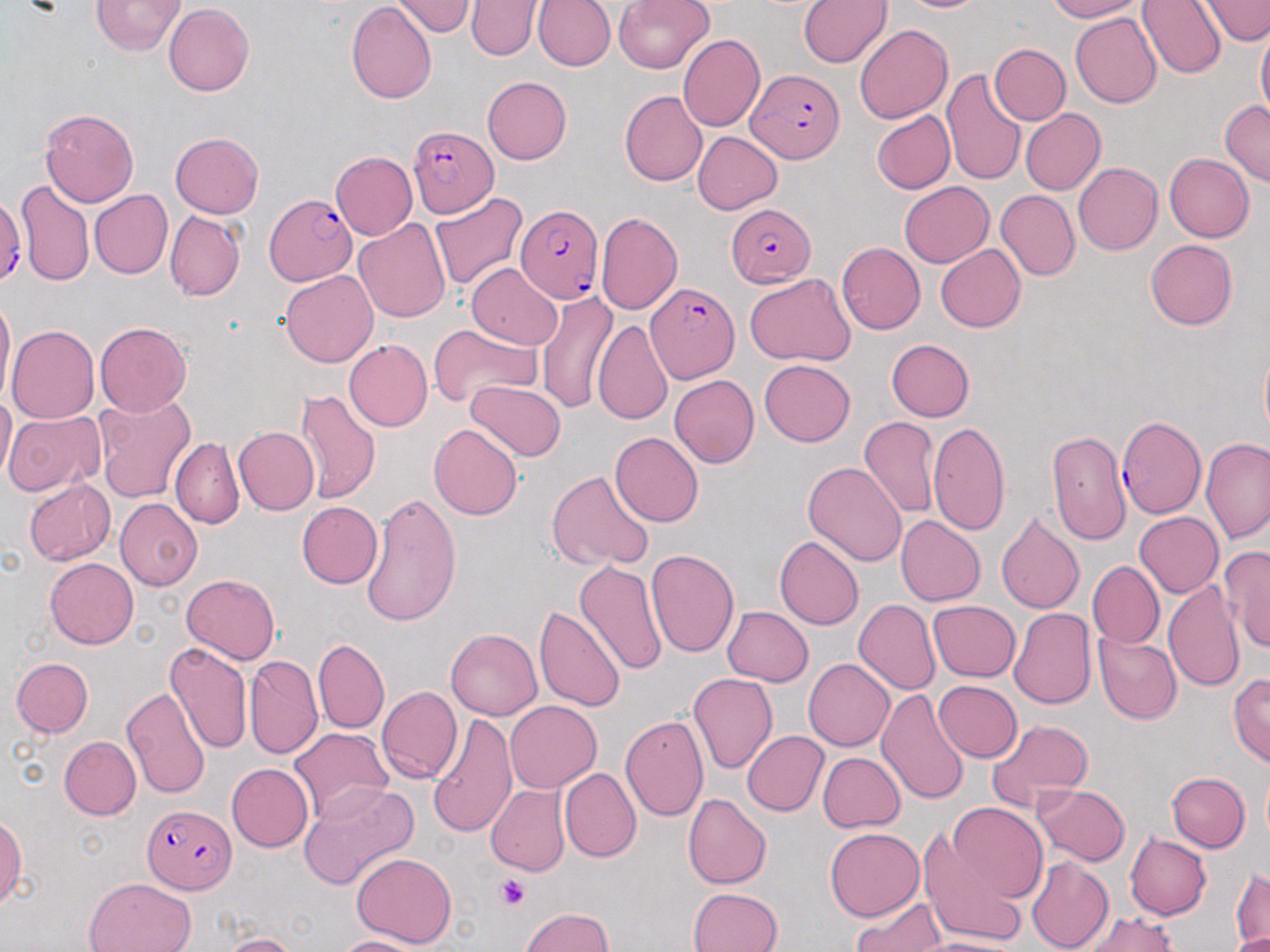
slide-level diagnosis = Plasmodium falciparum
field of view = one of a larger specimen
Plasmodium falciparum-infected red blood cell locations = approximate bounding boxes as (x1, y1, x2, y2) in pixels: (747, 69, 844, 164), (406, 125, 497, 218), (265, 194, 356, 285), (0, 197, 24, 284), (515, 203, 604, 302), (726, 203, 816, 285), (644, 282, 738, 383), (1116, 416, 1205, 519), (139, 805, 235, 892)
platelet locations = approximate bounding boxes as (x1, y1, x2, y2) in pixels: (494, 872, 529, 911)
preparation = thin blood film
uninfected red blood cell locations = approximate bounding boxes as (x1, y1, x2, y2) in pixels: (391, 0, 475, 37), (533, 0, 615, 71), (612, 0, 715, 74), (798, 0, 893, 68), (897, 0, 990, 13), (1045, 0, 1145, 22), (1138, 0, 1227, 78), (1199, 0, 1270, 46), (91, 1, 186, 55), (346, 1, 437, 104), (465, 1, 540, 60), (163, 3, 254, 96), (1070, 13, 1162, 108), (853, 24, 952, 124), (1256, 25, 1270, 127), (677, 35, 764, 132), (989, 44, 1070, 125), (942, 69, 1027, 187), (482, 77, 572, 165), (620, 90, 707, 186), (1220, 100, 1270, 187), (41, 107, 139, 207), (1020, 109, 1106, 195), (872, 110, 955, 194), (692, 130, 781, 214), (170, 131, 263, 217), (331, 150, 417, 241), (1164, 153, 1254, 242), (1073, 163, 1162, 255), (15, 179, 95, 288), (900, 182, 994, 267), (994, 189, 1079, 281), (89, 190, 172, 279), (429, 191, 527, 292), (165, 211, 245, 301), (595, 211, 683, 315), (354, 217, 451, 324), (1145, 239, 1238, 331), (837, 242, 925, 336), (936, 245, 1026, 332), (466, 264, 563, 349), (279, 270, 378, 368), (744, 273, 857, 368), (537, 289, 618, 415), (0, 294, 16, 406), (591, 320, 671, 425), (94, 322, 192, 417), (429, 323, 542, 411), (6, 325, 99, 424), (343, 339, 432, 432), (886, 339, 974, 422), (1260, 347, 1270, 442), (759, 359, 854, 447), (670, 375, 760, 468), (465, 379, 568, 462), (296, 389, 380, 502), (0, 393, 17, 482), (92, 394, 195, 503), (3, 410, 108, 498), (860, 414, 941, 519), (928, 421, 1010, 536), (429, 424, 523, 520), (233, 427, 319, 516), (1047, 429, 1130, 545), (610, 431, 703, 529), (171, 436, 244, 530), (1202, 437, 1270, 542), (802, 461, 907, 566), (546, 470, 654, 571), (23, 478, 115, 565), (358, 491, 461, 630), (115, 497, 203, 590), (296, 501, 383, 588), (995, 510, 1085, 615), (1134, 511, 1224, 597), (895, 515, 986, 606), (774, 535, 864, 630), (1220, 545, 1270, 652), (645, 549, 740, 658), (44, 558, 138, 648), (574, 559, 668, 677), (1088, 560, 1164, 648), (181, 573, 280, 664), (1163, 579, 1244, 693), (853, 599, 940, 695), (928, 600, 1020, 681), (534, 605, 625, 713), (723, 606, 813, 686), (1009, 608, 1097, 709), (446, 629, 542, 721), (1093, 633, 1181, 724), (313, 639, 389, 734), (164, 642, 252, 754), (244, 655, 323, 759), (12, 657, 93, 737), (803, 658, 895, 751), (1228, 671, 1270, 766), (688, 674, 778, 775), (933, 680, 1022, 763), (121, 686, 211, 798), (376, 686, 462, 784), (874, 690, 971, 805), (506, 700, 602, 793), (427, 713, 519, 838), (620, 714, 709, 821), (986, 717, 1095, 810), (288, 727, 392, 819), (741, 731, 828, 816), (58, 736, 141, 820), (818, 751, 906, 832), (226, 763, 314, 852), (559, 767, 641, 862), (1166, 772, 1250, 852), (1262, 772, 1270, 842), (299, 782, 419, 891), (487, 784, 570, 876), (1033, 784, 1130, 866), (684, 793, 771, 889), (947, 803, 1047, 903), (0, 816, 26, 908), (825, 827, 924, 921), (918, 829, 1029, 952), (1125, 834, 1211, 920), (352, 852, 458, 948), (1026, 856, 1113, 952), (1231, 867, 1268, 949), (85, 878, 194, 952), (688, 887, 782, 952), (851, 897, 946, 952), (521, 906, 613, 952), (1079, 911, 1177, 952), (1227, 931, 1270, 951), (222, 933, 300, 952), (336, 936, 429, 952), (913, 937, 1021, 952)
modality = optical microscopy
magnification = 1000x
stain = May-Grünwald-Giemsa
image size = 1270×952 pixels